Assess the morphology of the red blood cells.
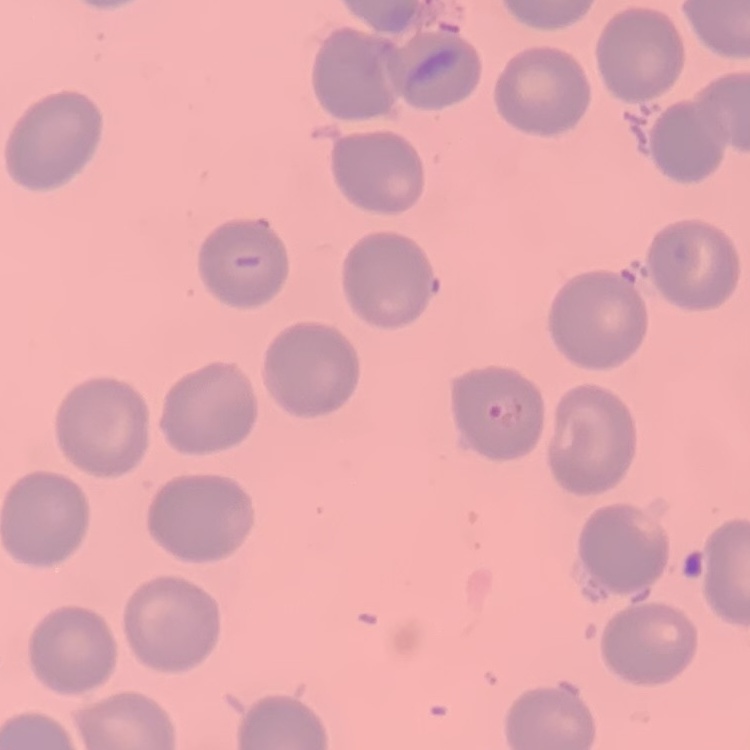
They show no rouleaux formation.

preparation = thin peripheral smear
image type = one tile cut from a larger photomicrograph
stain = Field's or Giemsa